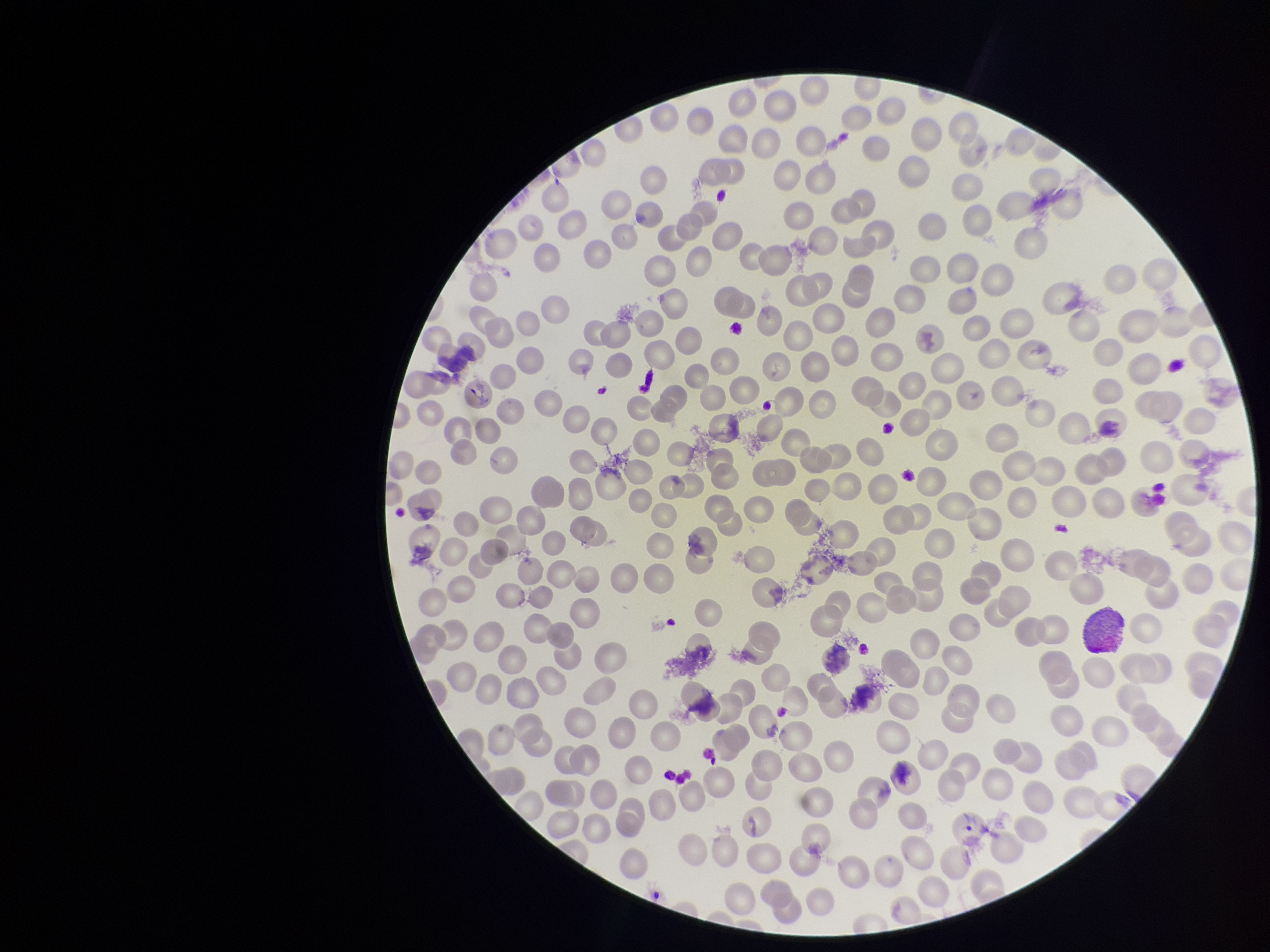 Parasitized red blood cell count: 0. Stained with Giemsa. Parasitized red blood cells: none identified. Patient malaria status: infected. Species reported for this patient: Plasmodium vivax. Red blood cell count: 272. Photographed through the microscope eyepiece with a smartphone camera. Preparation: thin. Image is 1270×952 pixels. One field from this slide.